State which cell type is depicted.
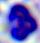
This is a leukocyte.

400x magnification. Micrograph.